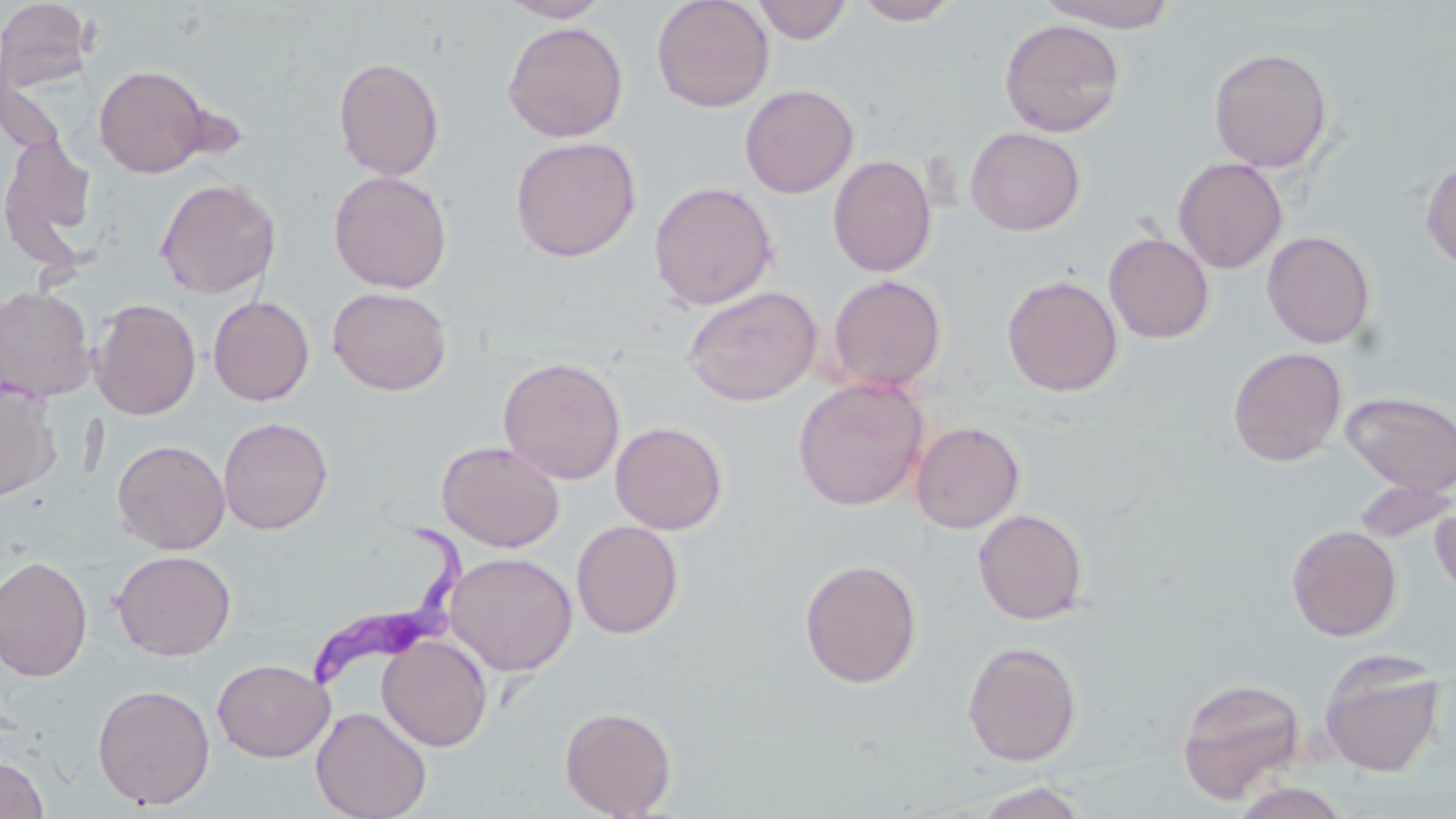

{
  "slide_level_diagnosis": "Trypanosoma brucei",
  "uninfected_red_blood_cell_locations": "approximate bounding boxes as [x1, y1, x2, y2] in pixels: [0, 0, 94, 93], [496, 0, 614, 23], [651, 0, 774, 113], [750, 0, 854, 44], [853, 0, 963, 26], [1036, 0, 1183, 32], [998, 18, 1126, 138], [501, 21, 629, 142], [1208, 46, 1334, 173], [332, 56, 445, 181], [93, 64, 211, 178], [739, 84, 859, 198], [965, 127, 1086, 236], [0, 131, 98, 269], [509, 135, 642, 263], [827, 154, 937, 278], [1172, 156, 1288, 274], [1420, 157, 1456, 272], [328, 170, 453, 293], [154, 177, 282, 300], [648, 181, 778, 310], [1262, 230, 1377, 349], [1103, 232, 1214, 343], [826, 274, 947, 393], [1002, 274, 1123, 396], [0, 285, 96, 402], [683, 285, 822, 407], [327, 286, 452, 395], [207, 295, 315, 406], [90, 298, 201, 420], [1227, 346, 1347, 467], [498, 356, 625, 485], [0, 377, 61, 503], [792, 377, 929, 512], [1340, 391, 1455, 500], [218, 416, 334, 535], [609, 421, 728, 535], [910, 421, 1025, 533], [112, 439, 230, 555], [436, 440, 565, 552], [1352, 475, 1453, 544], [1431, 497, 1456, 599], [973, 508, 1089, 625], [571, 520, 684, 639], [1285, 524, 1402, 641], [111, 550, 236, 661], [444, 551, 578, 677], [0, 555, 93, 682], [799, 558, 923, 689], [376, 634, 493, 752], [962, 641, 1083, 766], [1318, 650, 1445, 777], [212, 658, 335, 762], [1175, 676, 1307, 804], [92, 683, 216, 810], [310, 706, 432, 819], [559, 706, 677, 818], [0, 754, 50, 818], [969, 780, 1091, 818], [1230, 781, 1352, 819]",
  "image_size": "1456×819 pixels",
  "stain": "May-Grünwald-Giemsa",
  "modality": "optical microscopy",
  "magnification": "1000x",
  "preparation": "thin blood film",
  "field_of_view": "one of a larger specimen",
  "trypanosoma_brucei_locations": "approximate bounding boxes as [x1, y1, x2, y2] in pixels: [320, 513, 483, 686]"
}